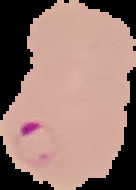
image type = segmented cell region on a black background
image size = 136×190 pixels
result = Plasmodium parasites identified
preparation = thin blood smear